Report the malaria status of this cell.
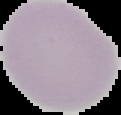

Uninfected.

preparation = thin blood film
image size = 121×115 pixels
image type = segmented cell region with the area outside set to black